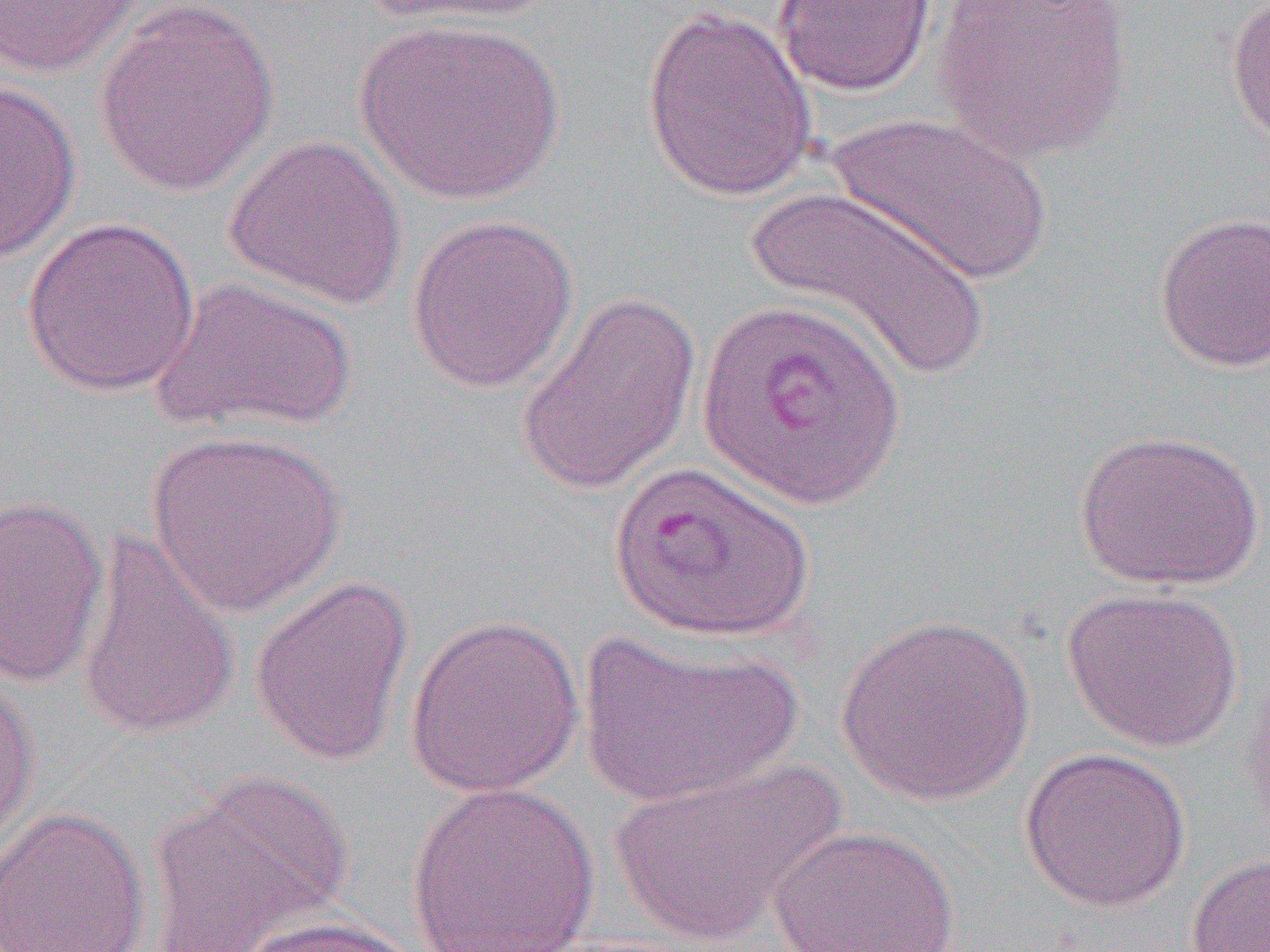

Summary:
  - Coordinate format: approximate bounding boxes as [x1, y1, x2, y2] in pixels
  - Uninfected red blood cell locations: [0, 0, 149, 78], [352, 0, 558, 29], [772, 0, 938, 98], [934, 0, 1132, 162], [1224, 0, 1270, 149], [93, 2, 280, 197], [641, 5, 818, 202], [355, 17, 565, 205], [0, 80, 82, 263], [830, 111, 1051, 284], [223, 134, 408, 311], [748, 186, 995, 383], [1153, 210, 1270, 373], [406, 213, 578, 394], [21, 217, 202, 397], [149, 277, 358, 435], [513, 289, 702, 498], [145, 428, 347, 616], [1074, 428, 1266, 591], [607, 460, 818, 644], [0, 492, 109, 688], [75, 528, 242, 742], [248, 575, 415, 767], [1062, 585, 1244, 753], [835, 611, 1036, 806], [404, 614, 585, 798], [574, 628, 804, 806], [0, 672, 41, 852], [1019, 745, 1191, 913], [607, 759, 846, 948], [146, 769, 352, 950], [405, 781, 600, 952], [0, 806, 151, 952], [770, 824, 961, 951], [1186, 853, 1270, 952], [234, 914, 424, 952]
  - Slide-level diagnosis: Plasmodium vivax
  - Magnification: 1000x
  - Image size: 1270×952 pixels
  - Field of view: single
  - Preparation: thin blood smear
  - Modality: optical microscopy